Point out each leukocyte.
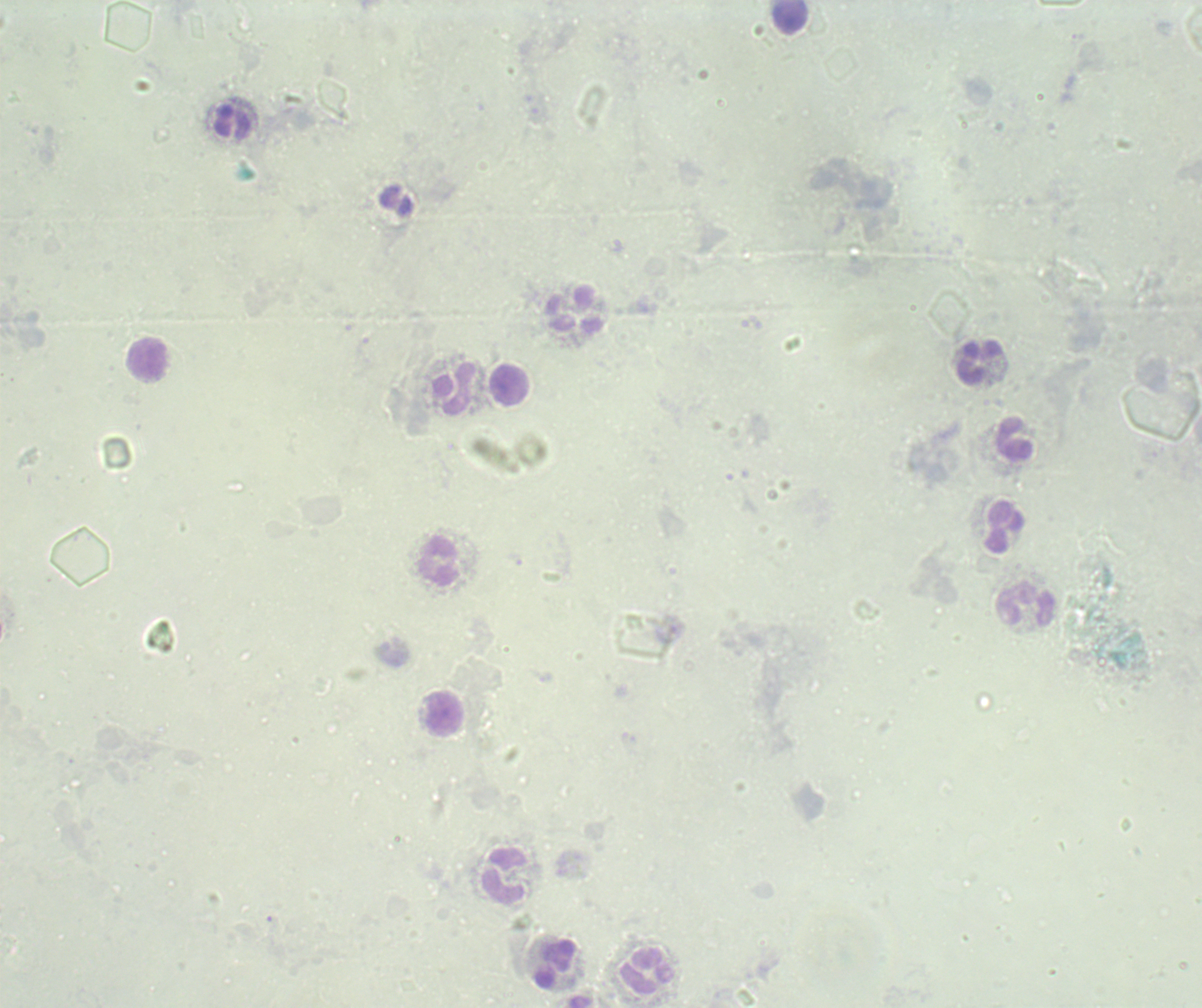
Approximate centers as (x, y) in pixels.
Leukocytes: (791, 15), (232, 121), (575, 310), (148, 360), (979, 362), (509, 385), (456, 389), (1015, 438), (1004, 526), (438, 562), (1025, 604), (444, 713), (504, 875), (554, 965), (647, 972).

Thick blood smear. Romanowsky-stained preparation. Result: no malaria parasites seen. Image is 1202×1008 pixels. 100x magnification. Single field of view. Previously used in an actual diagnosis. Background quality: unsatisfactory.